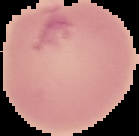 Segmented cell region on a black background. Result: negative for Plasmodium parasites. From a thin blood film. Image is 139×136 pixels.